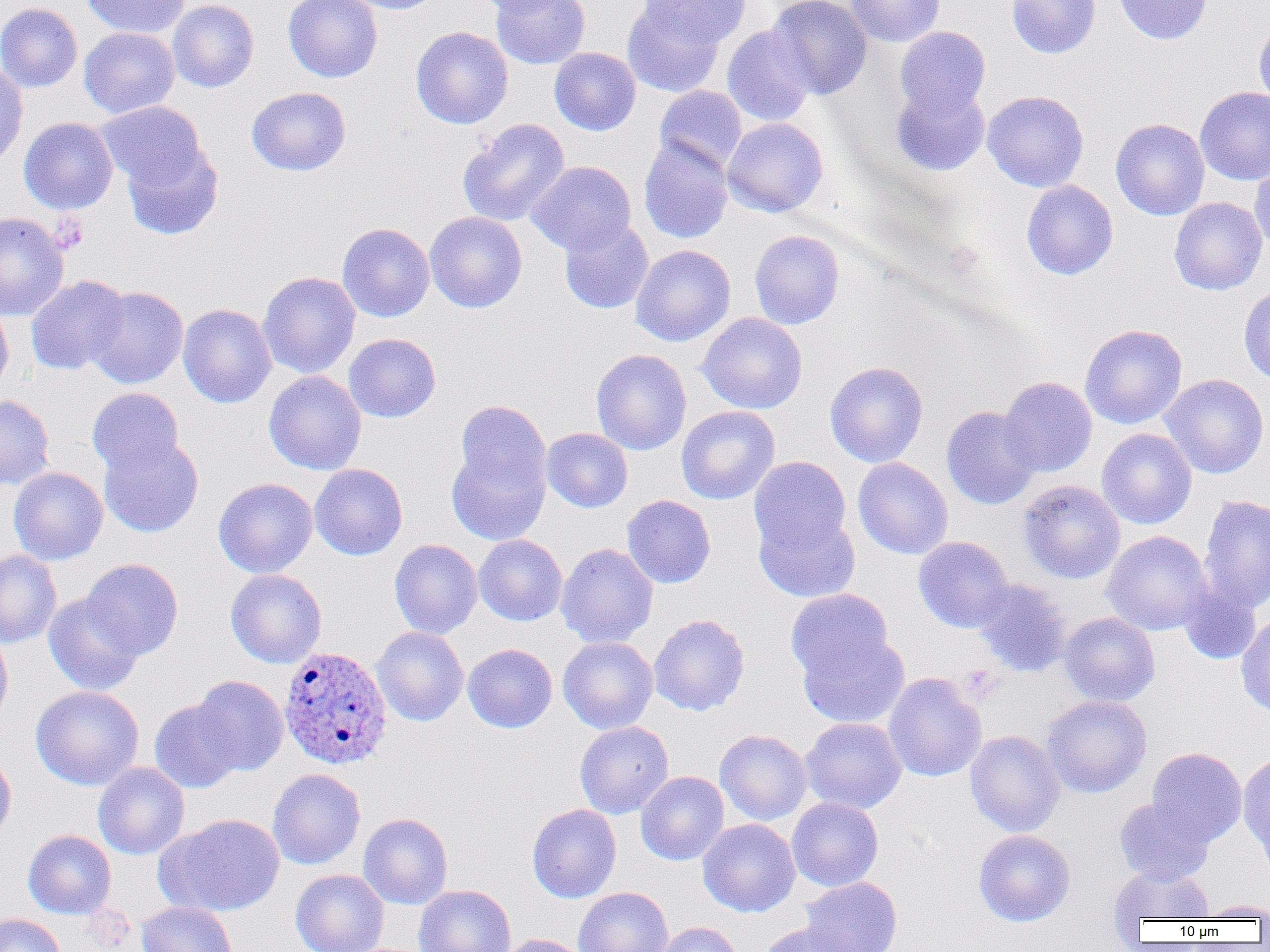
{
  "plasmodium_ovale_infected_red_blood_cell_locations": "approximate bounding boxes as named x1/y1/x2/y2 corners in pixels: (x1=278, y1=645, x2=393, y2=770)",
  "slide_level_diagnosis": "Plasmodium ovale",
  "platelet_locations": "approximate bounding boxes as named x1/y1/x2/y2 corners in pixels: (x1=49, y1=213, x2=87, y2=253)",
  "modality": "optical microscopy",
  "image_size": "1270×952 pixels",
  "preparation": "thin blood smear",
  "uninfected_red_blood_cell_locations": "approximate bounding boxes as named x1/y1/x2/y2 corners in pixels: (x1=80, y1=0, x2=190, y2=39), (x1=167, y1=0, x2=259, y2=92), (x1=283, y1=0, x2=382, y2=83), (x1=341, y1=0, x2=446, y2=14), (x1=471, y1=0, x2=567, y2=15), (x1=491, y1=0, x2=591, y2=70), (x1=637, y1=0, x2=751, y2=53), (x1=766, y1=0, x2=872, y2=99), (x1=845, y1=0, x2=944, y2=47), (x1=1007, y1=0, x2=1099, y2=58), (x1=1114, y1=0, x2=1213, y2=44), (x1=0, y1=2, x2=83, y2=92), (x1=621, y1=2, x2=727, y2=98), (x1=1253, y1=17, x2=1270, y2=112), (x1=722, y1=24, x2=816, y2=127), (x1=411, y1=26, x2=513, y2=129), (x1=894, y1=26, x2=991, y2=118), (x1=79, y1=27, x2=180, y2=118), (x1=549, y1=47, x2=641, y2=135), (x1=0, y1=61, x2=28, y2=169), (x1=891, y1=82, x2=990, y2=177), (x1=654, y1=85, x2=747, y2=172), (x1=246, y1=86, x2=351, y2=176), (x1=1195, y1=86, x2=1270, y2=186), (x1=982, y1=90, x2=1089, y2=192), (x1=96, y1=101, x2=205, y2=189), (x1=19, y1=117, x2=119, y2=214), (x1=722, y1=117, x2=828, y2=217), (x1=457, y1=118, x2=570, y2=227), (x1=1110, y1=118, x2=1210, y2=220), (x1=638, y1=137, x2=734, y2=244), (x1=122, y1=141, x2=223, y2=240), (x1=527, y1=160, x2=636, y2=255), (x1=1249, y1=161, x2=1270, y2=255), (x1=1021, y1=180, x2=1118, y2=280), (x1=1169, y1=197, x2=1267, y2=296), (x1=424, y1=211, x2=527, y2=313), (x1=0, y1=212, x2=70, y2=321), (x1=559, y1=218, x2=654, y2=314), (x1=337, y1=223, x2=435, y2=322), (x1=749, y1=229, x2=844, y2=329), (x1=630, y1=244, x2=736, y2=346), (x1=258, y1=271, x2=360, y2=379), (x1=25, y1=275, x2=130, y2=375), (x1=1239, y1=285, x2=1270, y2=386), (x1=85, y1=286, x2=188, y2=389), (x1=0, y1=301, x2=14, y2=397), (x1=177, y1=303, x2=277, y2=408), (x1=697, y1=313, x2=808, y2=414), (x1=1079, y1=323, x2=1187, y2=429), (x1=344, y1=333, x2=441, y2=423), (x1=591, y1=349, x2=692, y2=455), (x1=824, y1=361, x2=928, y2=467), (x1=264, y1=371, x2=366, y2=475), (x1=1159, y1=374, x2=1269, y2=479), (x1=999, y1=376, x2=1097, y2=477), (x1=86, y1=387, x2=185, y2=477), (x1=0, y1=394, x2=55, y2=491), (x1=455, y1=399, x2=551, y2=500), (x1=676, y1=405, x2=780, y2=505), (x1=941, y1=405, x2=1041, y2=509), (x1=542, y1=428, x2=632, y2=512), (x1=1096, y1=428, x2=1196, y2=529), (x1=98, y1=433, x2=204, y2=537), (x1=447, y1=440, x2=550, y2=546), (x1=748, y1=456, x2=852, y2=557), (x1=852, y1=457, x2=953, y2=559), (x1=309, y1=463, x2=408, y2=560), (x1=8, y1=467, x2=108, y2=565), (x1=213, y1=477, x2=317, y2=578), (x1=1018, y1=479, x2=1125, y2=584), (x1=1198, y1=494, x2=1270, y2=614), (x1=621, y1=495, x2=716, y2=588), (x1=754, y1=510, x2=860, y2=603), (x1=1101, y1=530, x2=1213, y2=635), (x1=474, y1=535, x2=567, y2=626), (x1=913, y1=536, x2=1014, y2=633), (x1=389, y1=539, x2=482, y2=639), (x1=556, y1=543, x2=658, y2=649), (x1=0, y1=549, x2=62, y2=648), (x1=81, y1=558, x2=184, y2=659), (x1=225, y1=569, x2=326, y2=668), (x1=972, y1=578, x2=1074, y2=677), (x1=1178, y1=584, x2=1262, y2=665), (x1=785, y1=588, x2=893, y2=684), (x1=43, y1=593, x2=146, y2=696), (x1=1059, y1=612, x2=1160, y2=706), (x1=649, y1=614, x2=750, y2=716), (x1=1235, y1=614, x2=1270, y2=719), (x1=0, y1=626, x2=14, y2=729), (x1=371, y1=626, x2=469, y2=726), (x1=796, y1=631, x2=909, y2=728), (x1=558, y1=636, x2=658, y2=734), (x1=462, y1=643, x2=558, y2=733), (x1=883, y1=672, x2=987, y2=782), (x1=191, y1=675, x2=289, y2=776), (x1=30, y1=685, x2=144, y2=790), (x1=1041, y1=695, x2=1152, y2=797), (x1=149, y1=699, x2=243, y2=793), (x1=800, y1=717, x2=907, y2=814), (x1=574, y1=721, x2=674, y2=818), (x1=714, y1=729, x2=813, y2=825), (x1=964, y1=730, x2=1065, y2=837), (x1=1146, y1=747, x2=1247, y2=846), (x1=0, y1=750, x2=16, y2=844), (x1=1238, y1=753, x2=1270, y2=858), (x1=93, y1=762, x2=189, y2=860), (x1=267, y1=768, x2=365, y2=869), (x1=636, y1=771, x2=729, y2=865), (x1=787, y1=797, x2=883, y2=892), (x1=1114, y1=797, x2=1216, y2=886), (x1=527, y1=804, x2=621, y2=903), (x1=358, y1=813, x2=453, y2=909), (x1=156, y1=814, x2=285, y2=917), (x1=698, y1=818, x2=800, y2=917), (x1=23, y1=830, x2=116, y2=919), (x1=973, y1=830, x2=1075, y2=927), (x1=1109, y1=865, x2=1214, y2=923), (x1=291, y1=869, x2=389, y2=952), (x1=799, y1=877, x2=902, y2=952), (x1=414, y1=884, x2=516, y2=952), (x1=574, y1=887, x2=673, y2=952), (x1=1195, y1=900, x2=1270, y2=920), (x1=136, y1=901, x2=238, y2=952), (x1=0, y1=913, x2=67, y2=952), (x1=654, y1=921, x2=743, y2=952), (x1=757, y1=922, x2=858, y2=952), (x1=498, y1=934, x2=589, y2=952)",
  "field_of_view": "single",
  "magnification": "1000x"
}